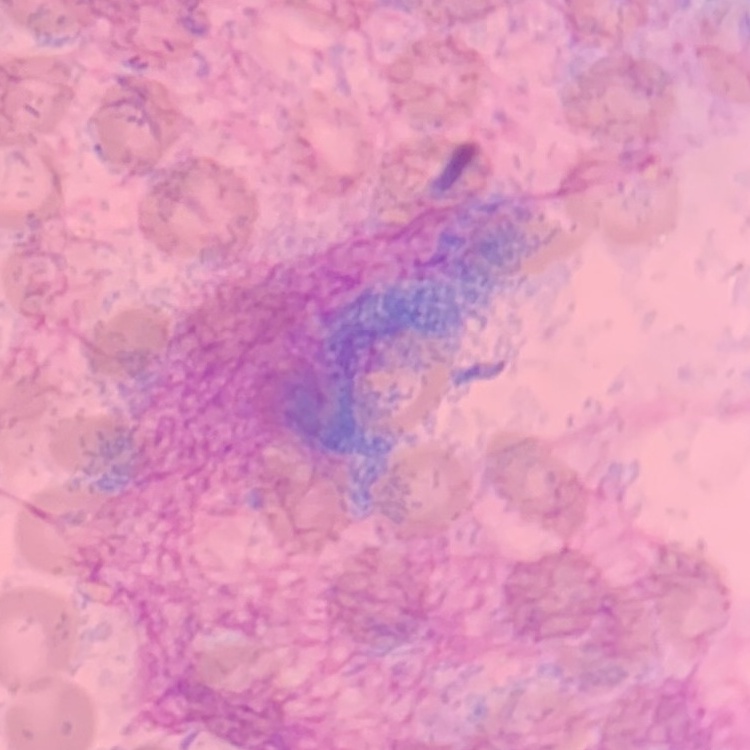

erythrocyte morphology = no rouleaux formation
preparation = thin blood smear
stain = Field's or Giemsa
image type = square crop of a larger photomicrograph